Give the preparation type.
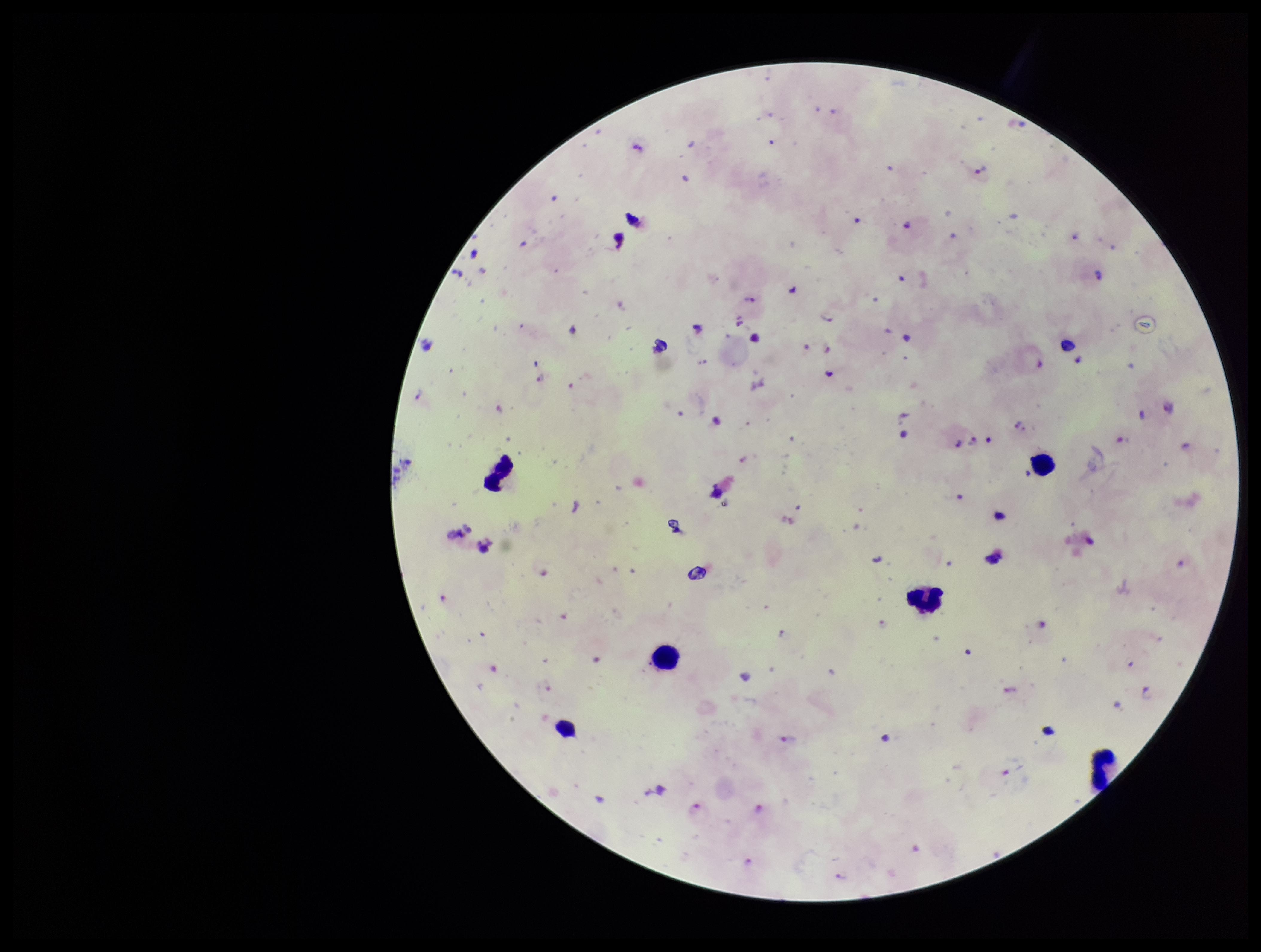
Thick.

Single field of view. Species reported for this patient: Plasmodium falciparum. Stained with Giemsa. Image is 1261×952 pixels. Parasite count: 31. Photographed through the microscope eyepiece with a smartphone camera. Plasmodium parasites: identified. Leukocyte count: 5. Patient malaria status: positive.